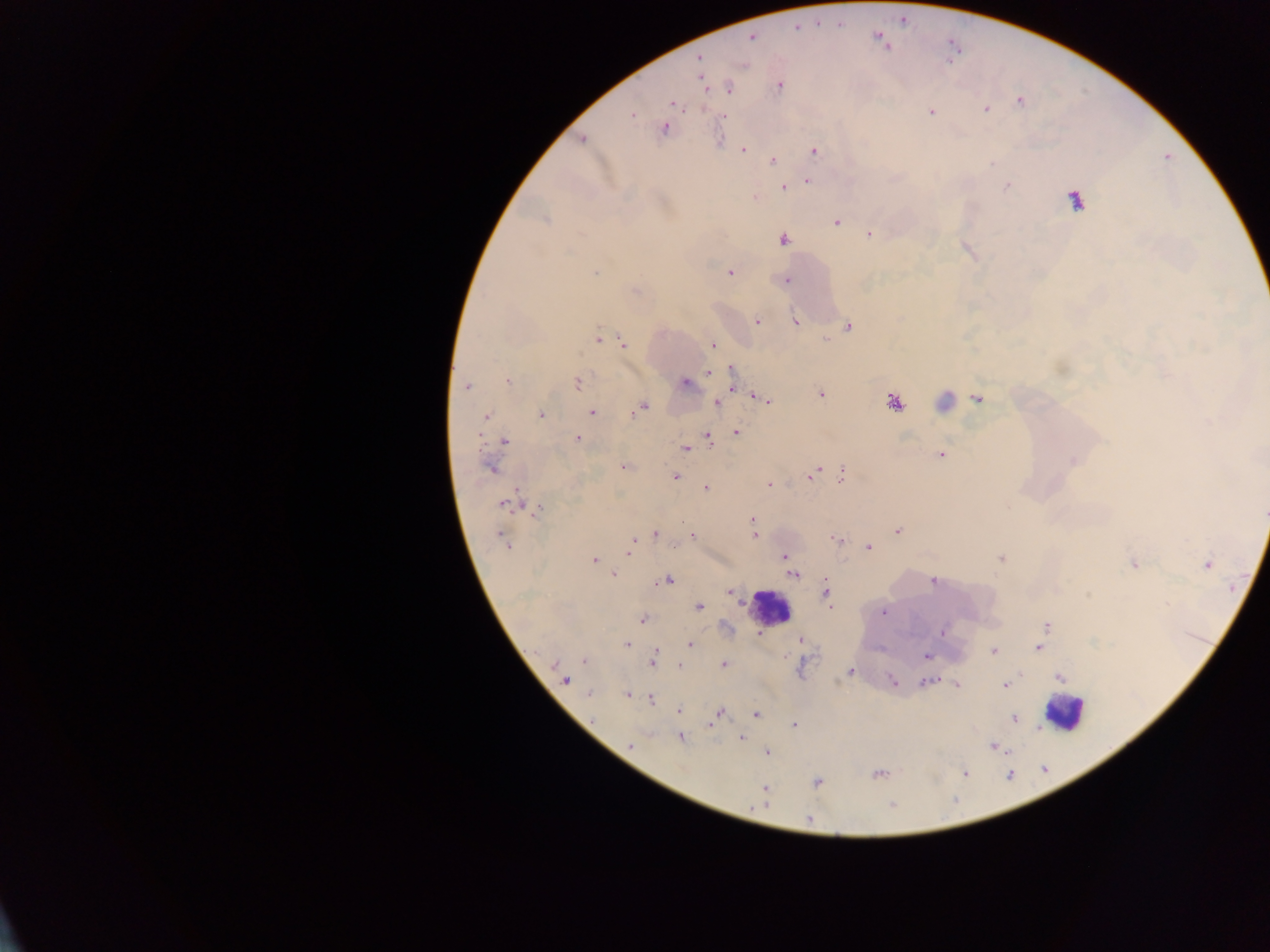

Approximate centers as [x, y] in pixels.
Summary:
  - Malaria parasite locations: [750, 37], [700, 57], [700, 74], [702, 82], [780, 86], [729, 88], [1020, 102], [672, 103], [986, 109], [931, 112], [632, 115], [724, 117], [664, 129], [583, 139], [743, 150], [813, 151], [772, 160], [807, 181], [1007, 186], [784, 188], [754, 198], [1075, 201], [545, 220], [837, 222], [870, 235], [783, 240], [730, 272], [595, 273], [787, 280], [757, 322], [796, 323], [848, 326], [597, 339], [825, 340], [623, 342], [713, 345], [709, 372], [731, 375], [508, 381], [577, 383], [685, 383], [466, 387], [821, 394], [977, 399], [763, 400], [894, 402], [717, 403], [642, 408], [591, 411], [541, 415], [487, 416], [736, 433], [708, 436], [578, 438], [505, 441], [685, 449], [940, 454], [1073, 461], [623, 467], [490, 468], [841, 473], [811, 475], [675, 477], [769, 484], [705, 489], [507, 503], [538, 510], [1263, 513], [752, 520], [897, 531], [655, 533], [755, 535], [692, 536], [502, 538], [837, 539], [506, 544], [630, 547], [868, 548], [785, 556], [1001, 558], [594, 560], [1134, 564], [1207, 564], [613, 574], [793, 575], [668, 580], [933, 581], [730, 591], [825, 593], [828, 600], [699, 607], [883, 612], [642, 620], [1046, 627], [943, 632], [800, 640], [627, 644], [690, 644], [1039, 648], [993, 651], [655, 654], [926, 656], [584, 660], [653, 661], [724, 664], [680, 666], [851, 671], [1059, 677], [565, 680], [892, 682], [926, 683], [957, 685], [1005, 685], [589, 694], [627, 695], [650, 699], [679, 710], [718, 713], [756, 714], [1014, 719], [711, 725], [795, 725], [741, 737], [681, 738], [631, 745], [994, 747], [767, 752], [965, 773], [879, 774], [817, 783], [764, 789], [758, 806], [892, 806], [809, 818]
  - Leukocyte locations: [769, 607], [1064, 712]
  - Country: Ghana
  - Image size: 1270×952 pixels
  - Preparation: thick blood smear
  - Capture: mobile-phone photograph through a microscope
  - Field of view: single